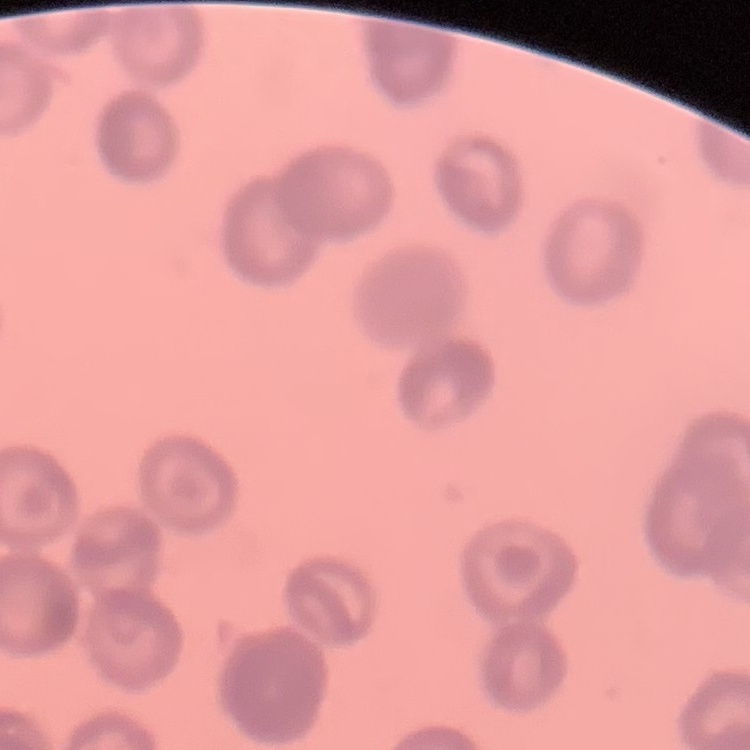
Summary:
  - Red blood cell morphology: rouleaux formation
  - Image type: square crop of a larger photomicrograph
  - Preparation: thin peripheral smear
  - Stain: Field's or Giemsa